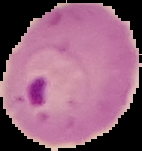

result = malaria parasites identified
image type = segmented cell region with the area outside set to black
image size = 142×151 pixels
preparation = thin blood smear